Report the malaria status of this cell.
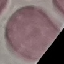

It is uninfected.

capture = smartphone camera at the microscope eyepiece
preparation = thin smear
stain = Giemsa
image type = cell patch, automatically extracted from a larger field of view and resized to 64 × 64 pixels